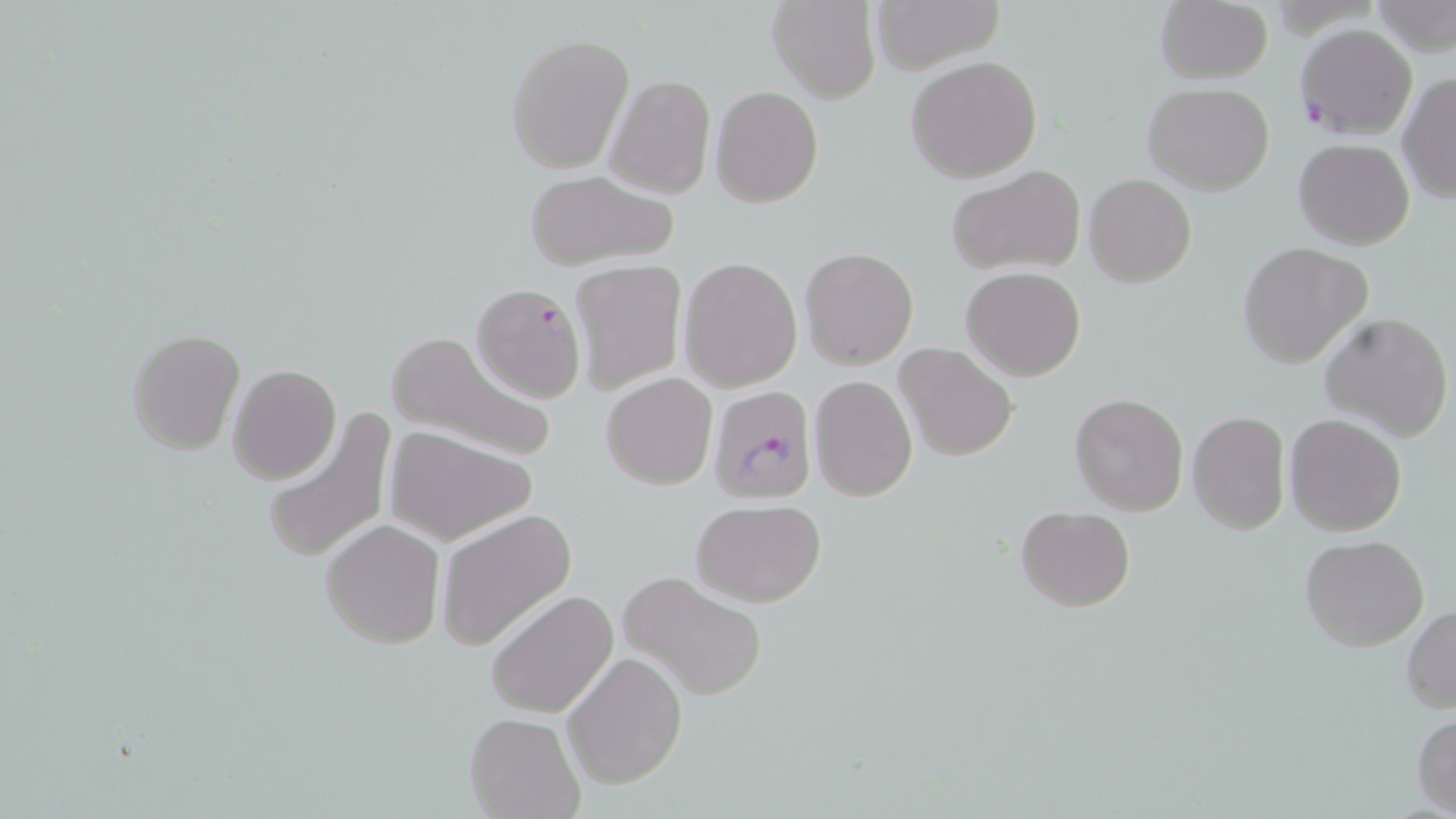

{
  "slide_level_diagnosis": "Plasmodium falciparum",
  "stain": "May-Grünwald-Giemsa",
  "modality": "light microscopy",
  "preparation": "thin blood smear",
  "field_of_view": "single",
  "plasmodium_falciparum_infected_red_blood_cell_locations": "approximate bounding boxes as (x1, y1, x2, y2) in pixels: (1294, 23, 1419, 140), (469, 282, 588, 404), (707, 383, 819, 504)",
  "uninfected_red_blood_cell_locations": "approximate bounding boxes as (x1, y1, x2, y2) in pixels: (869, 0, 1003, 73), (767, 1, 881, 103), (1368, 1, 1456, 60), (1154, 2, 1273, 84), (506, 31, 635, 175), (904, 55, 1044, 182), (605, 73, 715, 200), (1397, 73, 1456, 204), (1142, 82, 1276, 195), (711, 85, 824, 209), (1293, 137, 1416, 249), (943, 164, 1086, 276), (522, 170, 681, 271), (1085, 174, 1196, 287), (1236, 241, 1371, 368), (799, 246, 919, 370), (677, 256, 802, 394), (571, 259, 687, 393), (960, 265, 1087, 381), (1320, 312, 1453, 441), (127, 327, 245, 456), (385, 329, 558, 466), (894, 342, 1018, 461), (228, 364, 341, 483), (601, 373, 718, 490), (808, 374, 918, 500), (1069, 391, 1189, 516), (1187, 410, 1292, 537), (260, 411, 397, 563), (1284, 413, 1407, 537), (386, 427, 536, 545), (691, 499, 825, 604), (1015, 506, 1135, 612), (436, 510, 576, 652), (321, 518, 445, 649), (1300, 535, 1429, 651), (618, 572, 768, 700), (487, 588, 619, 720), (1403, 605, 1456, 713), (562, 652, 686, 789), (464, 710, 583, 818), (1411, 712, 1456, 815)",
  "magnification": "1000x",
  "image_size": "1456×819 pixels"
}